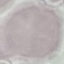

Summary:
  - Malaria status: uninfected
  - Stain: Giemsa
  - Preparation: thin blood smear
  - Capture: smartphone through the microscope eyepiece
  - Image type: automatically extracted cell patch, resized to 64 × 64 pixels